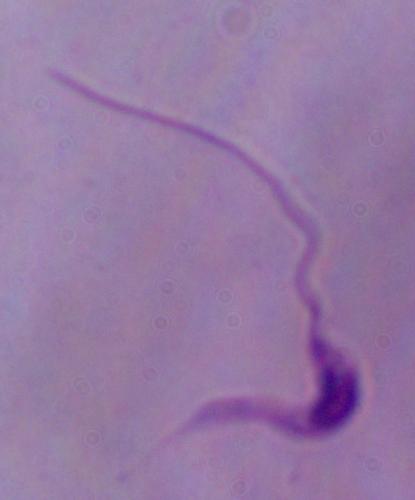
modality = photomicrograph
magnification = 1000x
identification = Leishmania